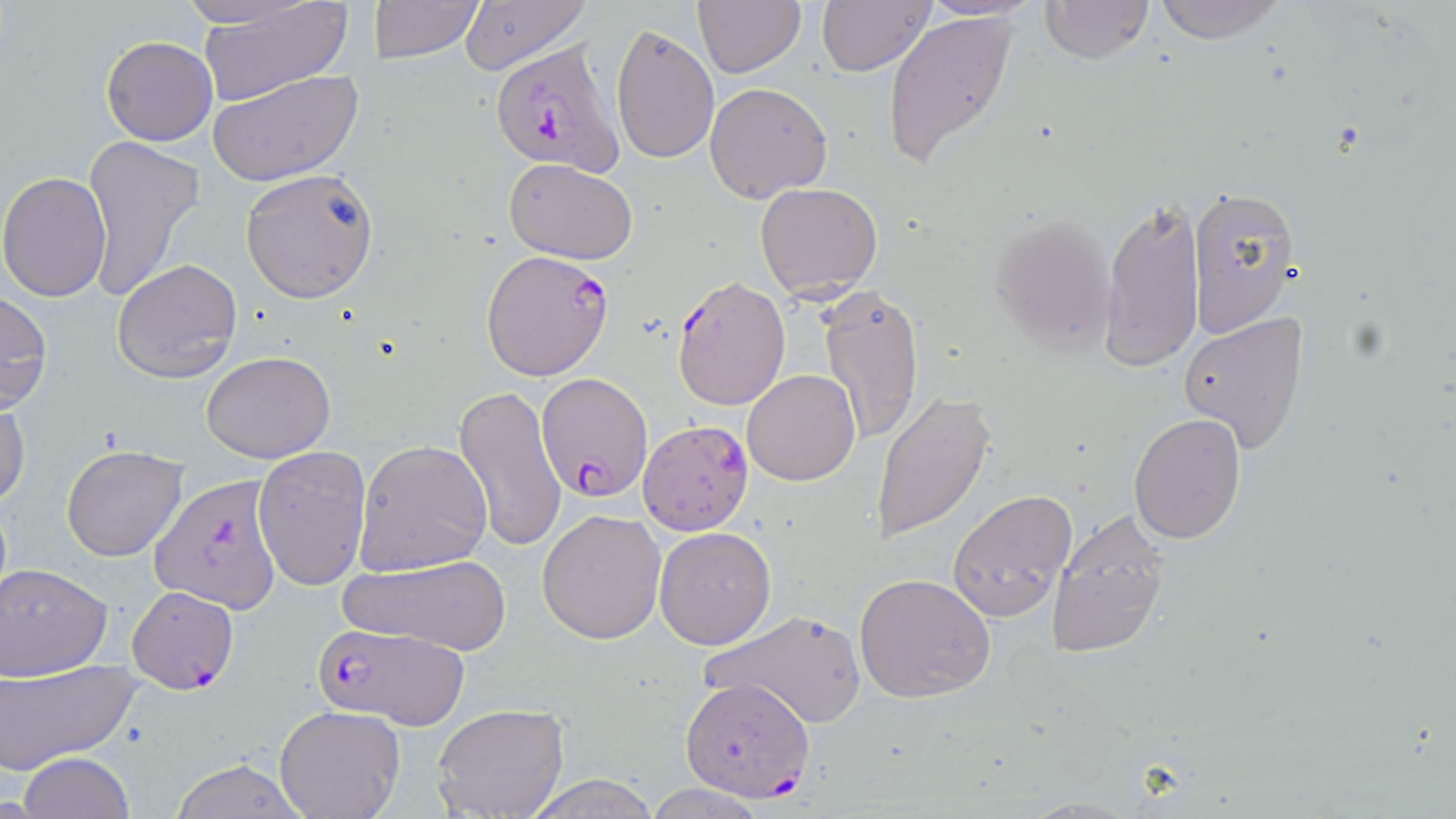

slide-level diagnosis = Plasmodium falciparum
magnification = 1000x
Plasmodium falciparum-infected red blood cell locations = approximate bounding boxes as named x1/y1/x2/y2 corners in pixels: (x1=491, y1=40, x2=621, y2=176), (x1=480, y1=250, x2=613, y2=381), (x1=673, y1=275, x2=791, y2=411), (x1=535, y1=371, x2=650, y2=500), (x1=638, y1=417, x2=754, y2=535), (x1=151, y1=472, x2=285, y2=615), (x1=125, y1=585, x2=239, y2=694), (x1=314, y1=623, x2=470, y2=726), (x1=680, y1=678, x2=813, y2=803)
stain = May-Grünwald-Giemsa
image size = 1456×819 pixels
field of view = single
modality = optical microscopy
uninfected red blood cell locations = approximate bounding boxes as named x1/y1/x2/y2 corners in pixels: (x1=176, y1=0, x2=321, y2=29), (x1=198, y1=0, x2=353, y2=108), (x1=372, y1=0, x2=484, y2=65), (x1=459, y1=0, x2=591, y2=74), (x1=692, y1=0, x2=806, y2=77), (x1=1038, y1=0, x2=1156, y2=65), (x1=1151, y1=0, x2=1289, y2=45), (x1=816, y1=1, x2=935, y2=75), (x1=881, y1=9, x2=1020, y2=172), (x1=610, y1=24, x2=719, y2=165), (x1=101, y1=35, x2=217, y2=146), (x1=207, y1=69, x2=364, y2=189), (x1=704, y1=80, x2=834, y2=203), (x1=79, y1=134, x2=207, y2=305), (x1=503, y1=159, x2=637, y2=265), (x1=240, y1=168, x2=381, y2=302), (x1=0, y1=170, x2=113, y2=301), (x1=755, y1=181, x2=883, y2=298), (x1=1186, y1=185, x2=1298, y2=339), (x1=1100, y1=194, x2=1204, y2=371), (x1=986, y1=210, x2=1116, y2=357), (x1=112, y1=257, x2=242, y2=383), (x1=819, y1=284, x2=924, y2=445), (x1=0, y1=289, x2=53, y2=414), (x1=1179, y1=312, x2=1310, y2=454), (x1=201, y1=351, x2=336, y2=462), (x1=742, y1=368, x2=860, y2=485), (x1=453, y1=384, x2=569, y2=554), (x1=870, y1=391, x2=994, y2=545), (x1=1, y1=397, x2=30, y2=510), (x1=1128, y1=413, x2=1246, y2=544), (x1=354, y1=439, x2=494, y2=574), (x1=61, y1=445, x2=188, y2=561), (x1=253, y1=445, x2=372, y2=592), (x1=948, y1=489, x2=1078, y2=624), (x1=1046, y1=506, x2=1169, y2=661), (x1=538, y1=509, x2=667, y2=646), (x1=654, y1=527, x2=777, y2=648), (x1=330, y1=553, x2=519, y2=657), (x1=1, y1=564, x2=112, y2=680), (x1=855, y1=572, x2=995, y2=704), (x1=699, y1=606, x2=869, y2=731), (x1=1, y1=658, x2=140, y2=773), (x1=429, y1=702, x2=571, y2=819), (x1=274, y1=706, x2=403, y2=819), (x1=18, y1=751, x2=136, y2=818), (x1=169, y1=757, x2=310, y2=819), (x1=527, y1=774, x2=659, y2=818), (x1=643, y1=783, x2=769, y2=818)
preparation = thin blood film